Comment on the morphology of the red blood cells.
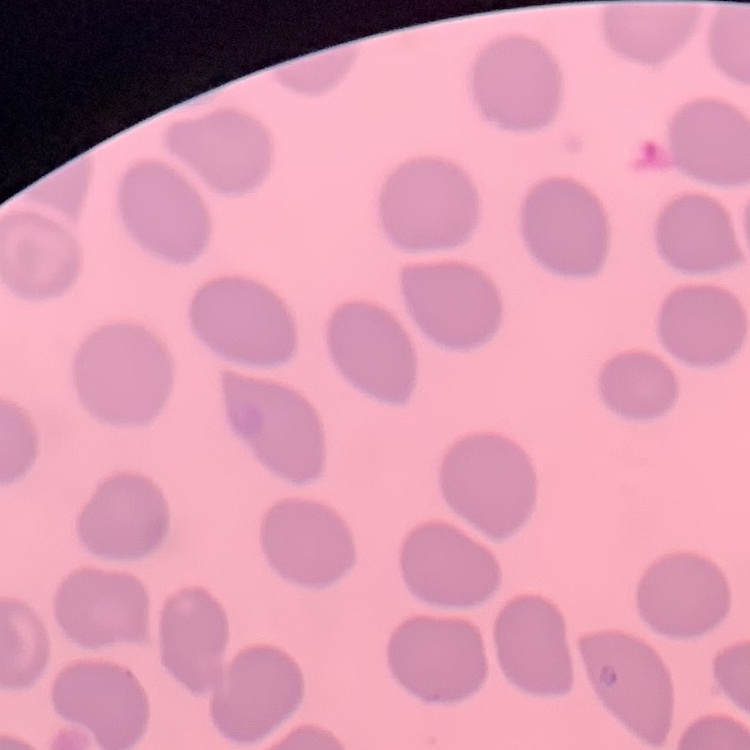

They show no rouleaux formation.

One tile cut from a larger photomicrograph. Thin blood film. Stained with either Field's or Giemsa.